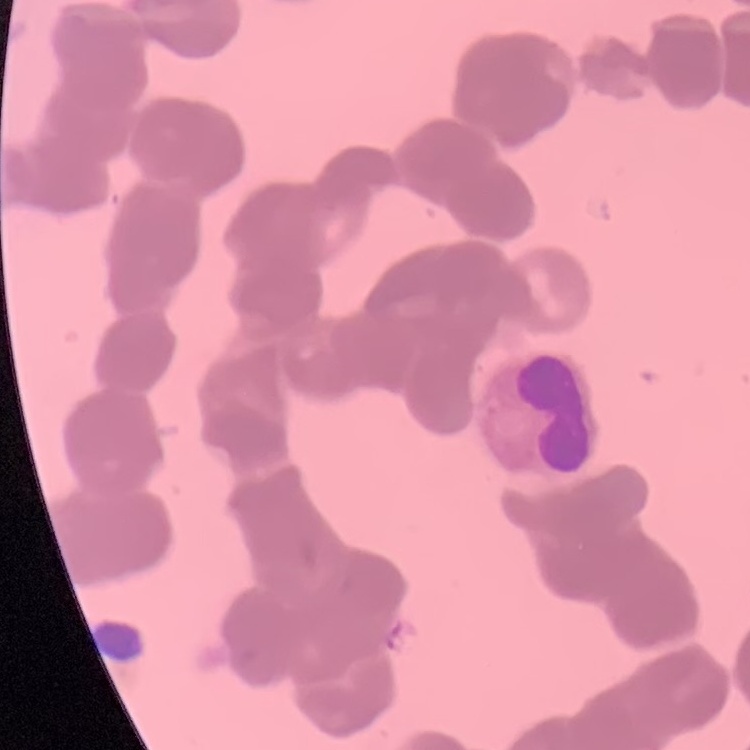

{
  "red_blood_cell_morphology": "rouleaux formation",
  "stain": "Field's or Giemsa",
  "image_type": "one tile cut from a larger photomicrograph",
  "preparation": "thin blood smear"
}